Report the malaria status of this cell.
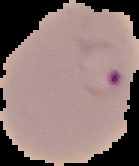

It is parasitized.

image_size: 139×166 pixels
preparation: thin blood film
image_type: segmented cell region on a black background